Locate and identify every blood parasite.
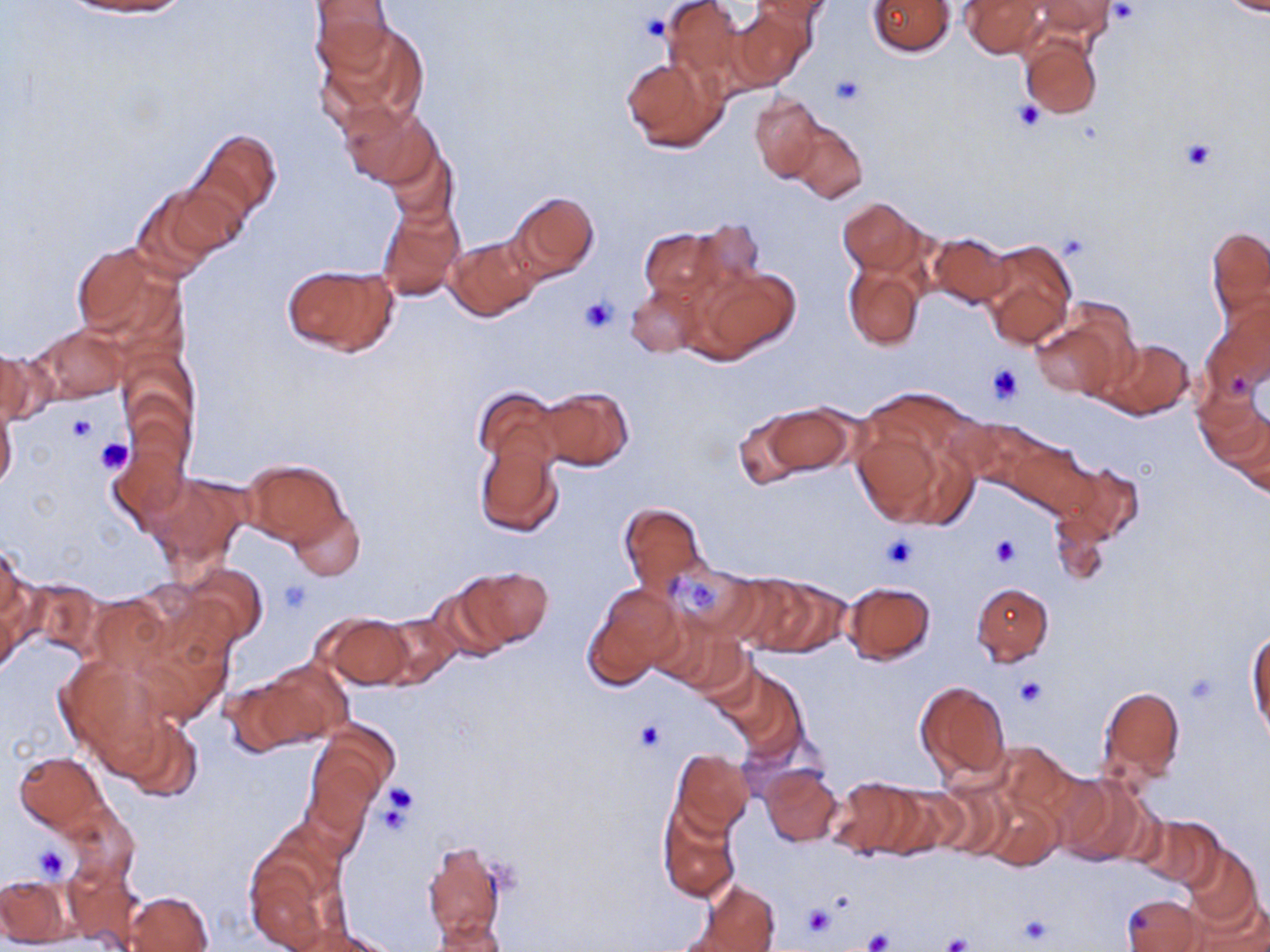

No blood parasites observed.

slide-level diagnosis = no evidence of blood parasites
preparation = thin blood film
platelet locations = approximate bounding boxes as (x1,y1)-(x2,y2) corner pairs in pixels: (1109,2)-(1141,25), (640,13)-(671,41), (830,75)-(864,107), (1012,99)-(1045,131), (1181,139)-(1216,170), (580,297)-(618,333), (987,364)-(1023,404), (65,412)-(97,444), (96,437)-(133,475), (883,535)-(917,569), (990,535)-(1019,566), (684,580)-(717,611), (278,581)-(313,615), (1186,672)-(1219,704), (1014,676)-(1048,708), (632,719)-(667,753), (381,781)-(418,822), (376,796)-(414,839), (32,844)-(70,882), (802,904)-(835,939), (1017,915)-(1055,946), (861,928)-(893,952), (941,934)-(971,952)
magnification = 1000x
stain = May-Grünwald-Giemsa
field of view = single
modality = light microscopy
image size = 1270×952 pixels
uninfected red blood cell locations = approximate bounding boxes as (x1,y1)-(x2,y2) corner pairs in pixels: (67,0)-(191,17), (662,0)-(753,90), (750,0)-(832,24), (1025,0)-(1119,39), (1216,0)-(1270,17), (308,1)-(394,74), (867,1)-(954,56), (962,1)-(1046,57), (727,8)-(813,91), (314,25)-(429,141), (1019,33)-(1101,119), (621,55)-(727,153), (750,92)-(824,182), (340,101)-(438,189), (785,120)-(867,202), (194,129)-(283,223), (381,136)-(458,229), (135,179)-(243,274), (507,190)-(599,282), (836,197)-(922,276), (377,200)-(465,302), (689,221)-(763,296), (1206,224)-(1270,324), (640,228)-(727,304), (927,231)-(1014,309), (447,237)-(540,322), (977,238)-(1077,350), (69,242)-(182,344), (280,263)-(399,358), (844,264)-(925,350), (692,267)-(802,363), (625,282)-(704,358), (1205,298)-(1270,392), (1031,310)-(1132,400), (34,324)-(129,402), (1095,338)-(1195,421), (0,346)-(40,429), (1195,384)-(1268,470), (538,385)-(633,471), (475,386)-(561,468), (0,399)-(18,493), (851,402)-(975,532), (748,404)-(856,481), (1227,414)-(1270,497), (956,419)-(1051,496), (113,430)-(191,526), (474,439)-(563,537), (1010,439)-(1094,518), (240,460)-(349,551), (1055,461)-(1144,547), (144,472)-(250,572), (618,502)-(707,597), (287,503)-(365,579), (1050,510)-(1113,586), (0,547)-(34,660), (179,563)-(268,649), (665,564)-(759,643), (456,566)-(552,651), (717,574)-(809,650), (752,576)-(850,658), (19,578)-(105,660), (424,581)-(515,663), (842,581)-(935,664), (587,582)-(682,687), (971,582)-(1053,665), (88,593)-(170,676), (131,612)-(237,726), (318,612)-(412,689), (375,612)-(461,691), (1246,628)-(1269,739), (55,654)-(169,764), (256,658)-(353,746), (721,668)-(807,763), (222,673)-(318,754), (915,681)-(1010,782), (1096,683)-(1187,789), (115,713)-(204,802), (308,725)-(396,821), (990,739)-(1081,823), (669,749)-(756,838), (14,752)-(106,833), (760,765)-(843,846), (1054,774)-(1152,867), (827,775)-(920,859), (925,779)-(1015,859), (877,782)-(969,858), (978,791)-(1061,870), (62,804)-(139,884), (657,806)-(740,905), (1135,815)-(1223,892), (421,840)-(508,946), (1180,843)-(1262,935), (245,846)-(342,952), (63,860)-(142,951), (1,874)-(77,947), (700,882)-(780,951), (1186,889)-(1269,952), (124,890)-(214,951), (1122,894)-(1204,952), (430,918)-(508,952), (289,926)-(399,952)